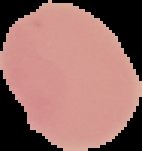

Image is 142×151 pixels. Malaria status: uninfected. Segmented cell region on a black background. From a thin blood smear.